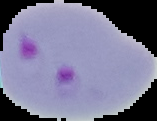
Summary:
  - Preparation: thin blood film
  - Image type: segmented cell region on a black background
  - Result: malaria parasites identified
  - Image size: 157×121 pixels